Classify this cell by malaria status.
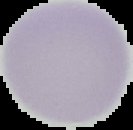

It is uninfected.

Cell region segmented out of the field of view; the surrounding area is masked to black. Image is 133×130 pixels. From a thin blood film.